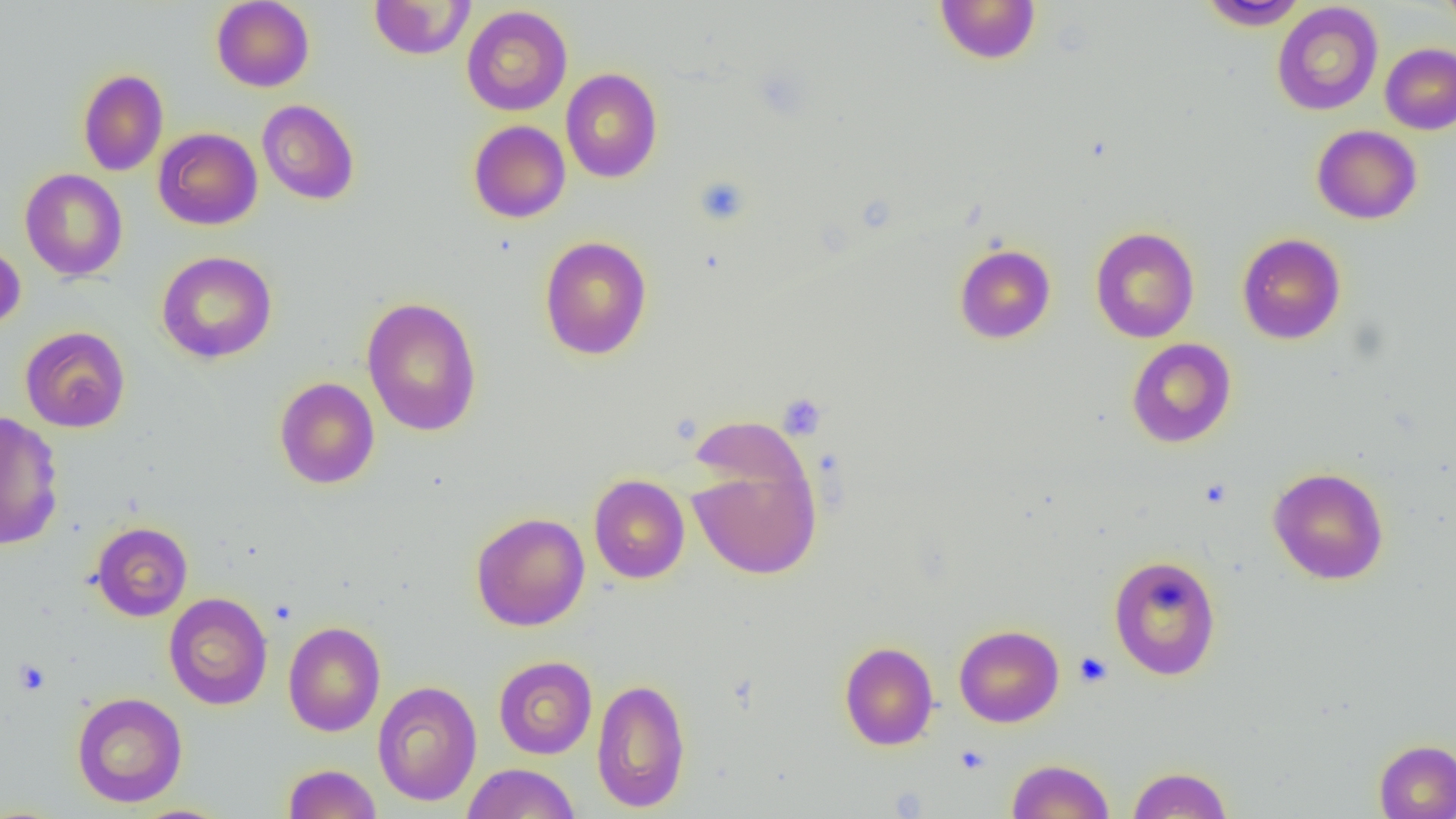

Approximate bounding boxes as named x1/y1/x2/y2 corners in pixels. Platelet locations: (x1=694, y1=176, x2=751, y2=226), (x1=779, y1=394, x2=826, y2=439), (x1=1073, y1=652, x2=1113, y2=688), (x1=13, y1=659, x2=50, y2=696), (x1=954, y1=744, x2=991, y2=775). Uninfected red blood cell locations: (x1=934, y1=0, x2=1042, y2=64), (x1=1440, y1=0, x2=1456, y2=35), (x1=211, y1=1, x2=315, y2=92), (x1=368, y1=1, x2=475, y2=60), (x1=1199, y1=1, x2=1310, y2=30), (x1=1271, y1=2, x2=1384, y2=116), (x1=461, y1=5, x2=573, y2=116), (x1=1380, y1=43, x2=1456, y2=134), (x1=561, y1=68, x2=663, y2=183), (x1=77, y1=69, x2=169, y2=176), (x1=257, y1=99, x2=360, y2=205), (x1=468, y1=120, x2=571, y2=223), (x1=1311, y1=125, x2=1422, y2=224), (x1=153, y1=127, x2=263, y2=230), (x1=20, y1=168, x2=128, y2=281), (x1=1090, y1=227, x2=1200, y2=343), (x1=1236, y1=233, x2=1346, y2=344), (x1=539, y1=236, x2=653, y2=360), (x1=0, y1=242, x2=26, y2=332), (x1=954, y1=243, x2=1056, y2=344), (x1=157, y1=251, x2=277, y2=364), (x1=361, y1=296, x2=483, y2=437), (x1=19, y1=326, x2=131, y2=433), (x1=1126, y1=338, x2=1237, y2=448), (x1=274, y1=377, x2=380, y2=489), (x1=0, y1=410, x2=65, y2=550), (x1=688, y1=454, x2=822, y2=580), (x1=1267, y1=467, x2=1389, y2=585), (x1=589, y1=474, x2=690, y2=584), (x1=470, y1=512, x2=590, y2=632), (x1=90, y1=521, x2=193, y2=621), (x1=1108, y1=554, x2=1222, y2=680), (x1=163, y1=592, x2=272, y2=710), (x1=283, y1=621, x2=385, y2=737), (x1=954, y1=624, x2=1064, y2=727), (x1=839, y1=641, x2=939, y2=751), (x1=493, y1=655, x2=597, y2=759), (x1=591, y1=677, x2=691, y2=813), (x1=372, y1=680, x2=483, y2=806), (x1=72, y1=691, x2=187, y2=808), (x1=1374, y1=739, x2=1456, y2=819), (x1=1006, y1=758, x2=1115, y2=818), (x1=282, y1=763, x2=382, y2=819), (x1=462, y1=763, x2=580, y2=819), (x1=1128, y1=765, x2=1233, y2=818). Slide-level diagnosis: no evidence of blood parasites. Image is 1456×819 pixels. Thin blood smear. Single field of view. Light microscopy. 1000x magnification.